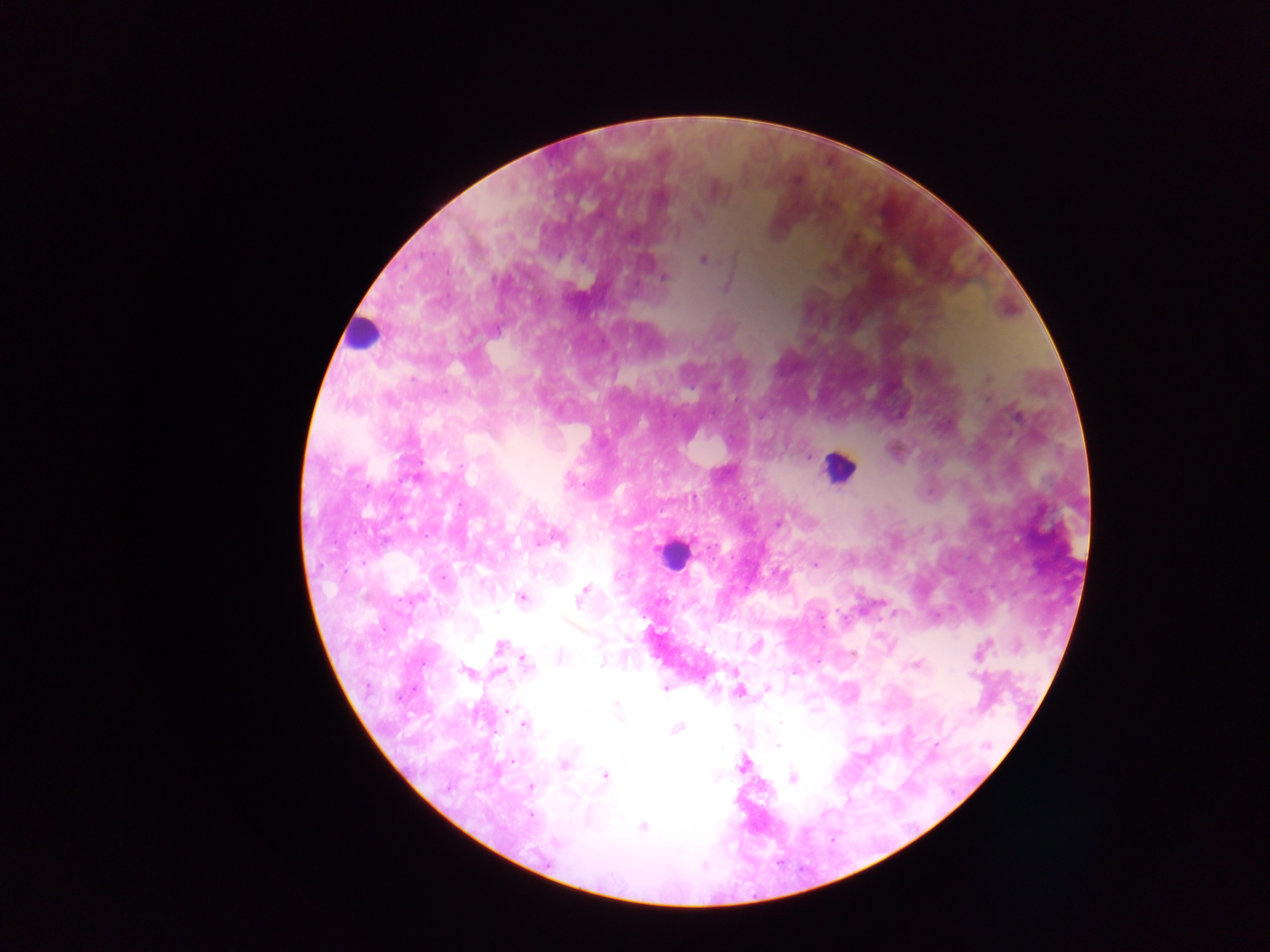
Approximate centers as x y in pixels.
Summary:
  - Leukocyte locations: 363 332; 839 468; 672 554
  - Malaria parasite locations: 661 198; 703 260; 664 277; 727 287; 412 379; 988 379; 1016 415; 808 457; 459 505; 778 524; 540 542; 815 564; 444 577; 583 592; 522 598; 580 598; 418 599; 496 611; 756 644; 986 644; 499 647; 560 656; 602 663; 526 664; 914 665; 466 672; 795 672; 973 676; 767 688; 665 690; 738 692; 616 705; 508 710; 619 715; 780 723; 524 724; 676 729; 777 745; 935 745; 987 745; 512 761; 563 764; 743 764; 606 776; 793 777; 716 778; 531 787; 531 816; 643 827; 555 841
  - Field of view: single
  - Country: Ghana
  - Capture: mobile-phone photograph through a microscope
  - Image size: 1270×952 pixels
  - Preparation: thick blood smear